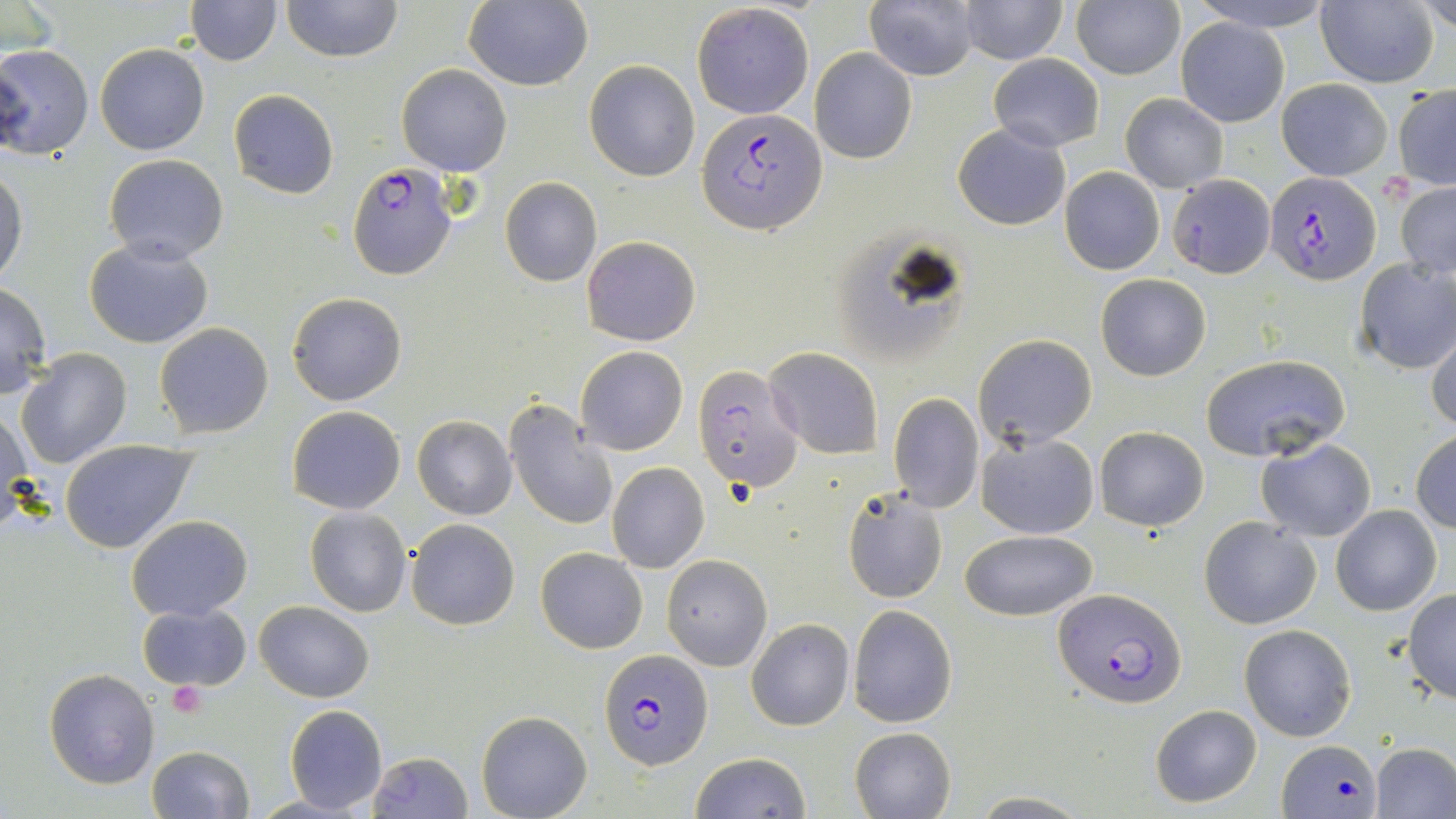
Approximate bounding boxes as [x1, y1, x2, y2] in pixels. Plasmodium falciparum-infected red blood cell locations: [699, 108, 826, 236], [347, 162, 458, 282], [1266, 171, 1379, 286], [692, 363, 802, 495], [1052, 589, 1184, 709], [599, 648, 713, 770], [1277, 738, 1380, 819]. Uninfected red blood cell locations: [184, 0, 282, 66], [280, 0, 403, 62], [1188, 0, 1338, 32], [1315, 0, 1438, 88], [463, 1, 593, 90], [1071, 1, 1183, 79], [1418, 1, 1455, 37], [866, 2, 980, 80], [957, 2, 1068, 64], [691, 4, 815, 118], [1174, 16, 1290, 126], [0, 43, 94, 161], [95, 44, 209, 155], [809, 48, 917, 163], [988, 54, 1104, 152], [584, 59, 700, 181], [397, 63, 511, 175], [1275, 78, 1393, 180], [1392, 85, 1456, 191], [228, 89, 339, 200], [1120, 93, 1228, 193], [953, 124, 1071, 230], [103, 153, 229, 265], [0, 164, 27, 287], [1060, 167, 1164, 276], [1168, 174, 1276, 277], [499, 177, 602, 287], [1394, 180, 1456, 280], [581, 235, 701, 347], [84, 239, 214, 349], [1353, 257, 1456, 374], [1095, 274, 1210, 382], [0, 283, 52, 398], [287, 292, 407, 406], [154, 322, 274, 439], [1426, 326, 1456, 434], [974, 334, 1097, 449], [575, 345, 688, 456], [15, 347, 133, 469], [765, 347, 884, 459], [1200, 351, 1351, 461], [888, 394, 984, 513], [505, 400, 618, 532], [1, 405, 31, 527], [287, 406, 406, 514], [412, 416, 517, 520], [1094, 426, 1209, 530], [1411, 430, 1456, 534], [976, 432, 1099, 539], [1256, 437, 1376, 542], [61, 439, 198, 553], [606, 463, 709, 572], [842, 486, 950, 604], [1332, 505, 1441, 616], [304, 507, 412, 616], [126, 515, 252, 621], [1199, 516, 1321, 630], [407, 518, 521, 631], [961, 531, 1098, 622], [536, 547, 647, 653], [661, 555, 771, 672], [1403, 590, 1456, 704], [254, 601, 374, 702], [138, 603, 252, 691], [849, 605, 957, 727], [747, 617, 854, 731], [1239, 623, 1358, 742], [44, 668, 159, 788], [1150, 704, 1262, 808], [284, 706, 387, 813], [477, 711, 592, 819], [849, 725, 957, 819], [1372, 743, 1456, 818], [147, 746, 254, 819], [366, 751, 474, 819], [688, 752, 811, 819], [969, 793, 1092, 817], [252, 795, 359, 817]. Platelet locations: [167, 679, 206, 718]. Slide-level diagnosis: Plasmodium falciparum. Thin blood smear. Image is 1456×819 pixels. May-Grünwald-Giemsa stain. 1000x magnification. Single field of view. Optical microscopy.